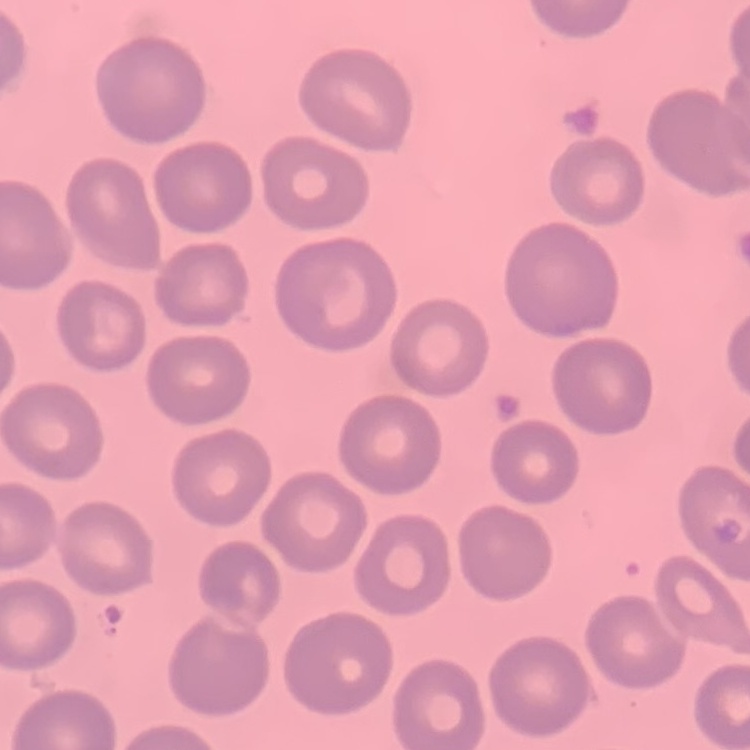

{
  "erythrocyte_morphology": "no rouleaux formation",
  "preparation": "thin blood smear",
  "image_type": "one tile cut from a larger photomicrograph",
  "stain": "Field's or Giemsa"
}